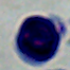

identification: white blood cell
magnification: 1000x
modality: photomicrograph